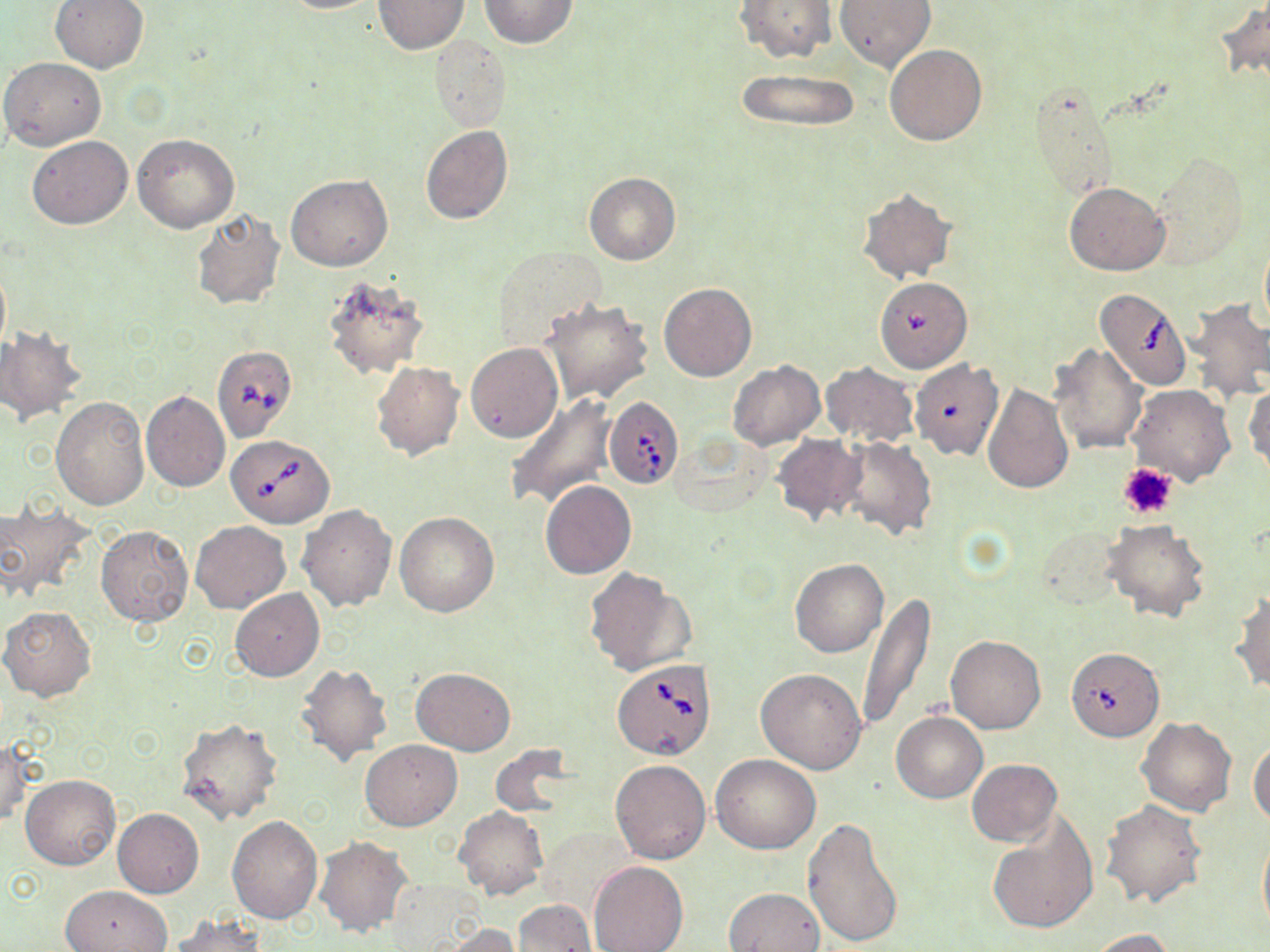
Approximate bounding boxes as (x1, y1, x2, y2) in pixels. Uninfected red blood cell locations: (50, 0, 150, 73), (273, 0, 384, 13), (374, 0, 468, 53), (479, 0, 576, 48), (736, 0, 836, 63), (834, 0, 935, 72), (1214, 0, 1270, 85), (428, 36, 510, 132), (885, 44, 986, 145), (2, 56, 106, 150), (734, 68, 862, 131), (1028, 83, 1119, 203), (421, 125, 513, 225), (133, 134, 239, 233), (27, 137, 132, 229), (1147, 151, 1250, 270), (583, 172, 680, 264), (287, 175, 392, 271), (1065, 181, 1170, 275), (857, 187, 957, 283), (189, 209, 288, 311), (1259, 236, 1270, 333), (492, 245, 605, 347), (0, 257, 10, 362), (322, 276, 429, 380), (658, 281, 757, 381), (1186, 298, 1270, 404), (538, 299, 653, 405), (0, 328, 85, 425), (1050, 342, 1148, 454), (465, 343, 563, 442), (908, 358, 1003, 461), (726, 360, 825, 450), (372, 361, 464, 460), (818, 362, 918, 447), (1245, 382, 1270, 477), (982, 384, 1073, 494), (1128, 385, 1234, 485), (141, 390, 230, 492), (504, 393, 620, 510), (51, 396, 149, 509), (670, 433, 774, 517), (771, 434, 865, 527), (837, 436, 938, 540), (540, 480, 637, 578), (0, 504, 95, 604), (297, 504, 397, 612), (394, 513, 500, 617), (191, 520, 291, 614), (1103, 520, 1210, 622), (96, 525, 194, 626), (1035, 525, 1123, 610), (790, 558, 889, 657), (583, 567, 695, 676), (231, 589, 325, 681), (1229, 592, 1270, 694), (858, 593, 934, 731), (0, 606, 96, 701), (946, 636, 1046, 733), (295, 663, 393, 767), (411, 667, 515, 755), (757, 668, 867, 772), (892, 712, 987, 803), (175, 716, 284, 827), (1137, 717, 1236, 815), (0, 736, 29, 828), (359, 739, 460, 830), (1249, 742, 1270, 828), (711, 755, 821, 854), (610, 759, 711, 863), (967, 759, 1061, 846), (747, 764, 880, 909), (20, 775, 120, 869), (1099, 799, 1207, 908), (455, 807, 547, 900), (113, 809, 204, 897), (227, 815, 323, 923), (802, 815, 904, 947), (986, 818, 1098, 934), (1257, 828, 1270, 939), (314, 836, 413, 937), (589, 860, 687, 952), (386, 879, 484, 947), (60, 885, 171, 951), (724, 887, 825, 952), (512, 900, 596, 951), (167, 915, 265, 952), (437, 924, 522, 951), (1086, 928, 1176, 952). Platelet locations: (1118, 463, 1179, 521). Babesia divergens-infected red blood cell locations: (874, 281, 970, 378), (1095, 287, 1192, 391), (212, 344, 297, 442), (604, 396, 684, 489), (226, 433, 334, 528), (1063, 645, 1165, 743), (613, 659, 716, 759). Slide-level diagnosis: Babesia divergens. Light microscopy. May-Grünwald-Giemsa stain. 1000x magnification. Thin blood smear. Image is 1270×952 pixels. One field of a larger specimen.